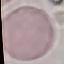

{
  "result": "negative for malaria parasites",
  "stain": "Giemsa",
  "capture": "smartphone through the microscope eyepiece",
  "preparation": "thin blood film",
  "image_type": "cell patch, automatically extracted from a larger field of view and resized to 64 × 64 pixels"
}